Report the malaria status of this cell.
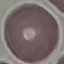
It is uninfected.

image type = cell patch, automatically extracted from a larger field of view and resized to 64 × 64 pixels
preparation = thin smear
capture = smartphone through the microscope eyepiece
stain = Giemsa